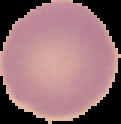
Summary:
  - Preparation: thin blood film
  - Image type: cell region segmented out of the field of view; surrounding area masked to black
  - Image size: 121×124 pixels
  - Result: no malaria parasites detected